Describe the morphology of the red blood cells.
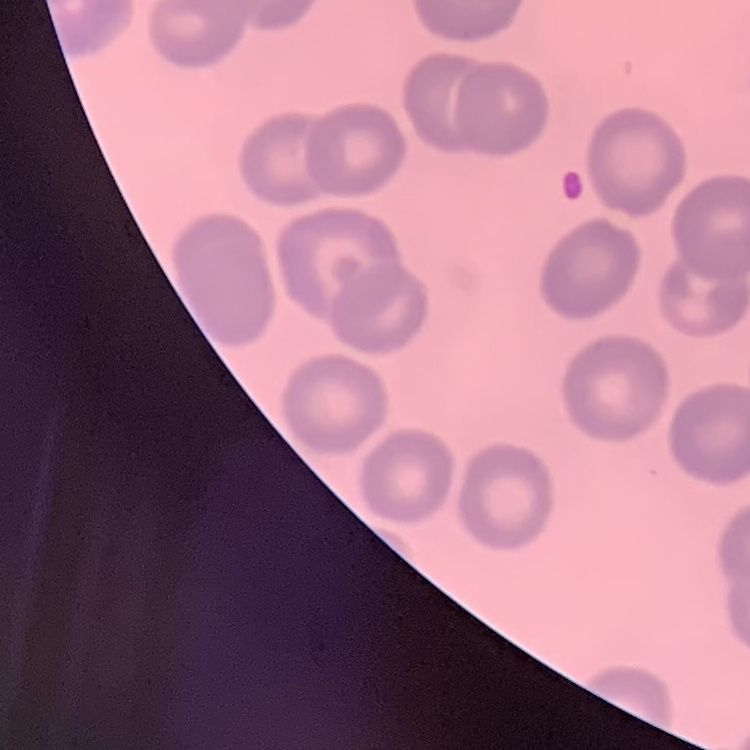
No rouleaux formation.

image type = square crop of a larger photomicrograph
stain = Field's or Giemsa
preparation = thin blood smear